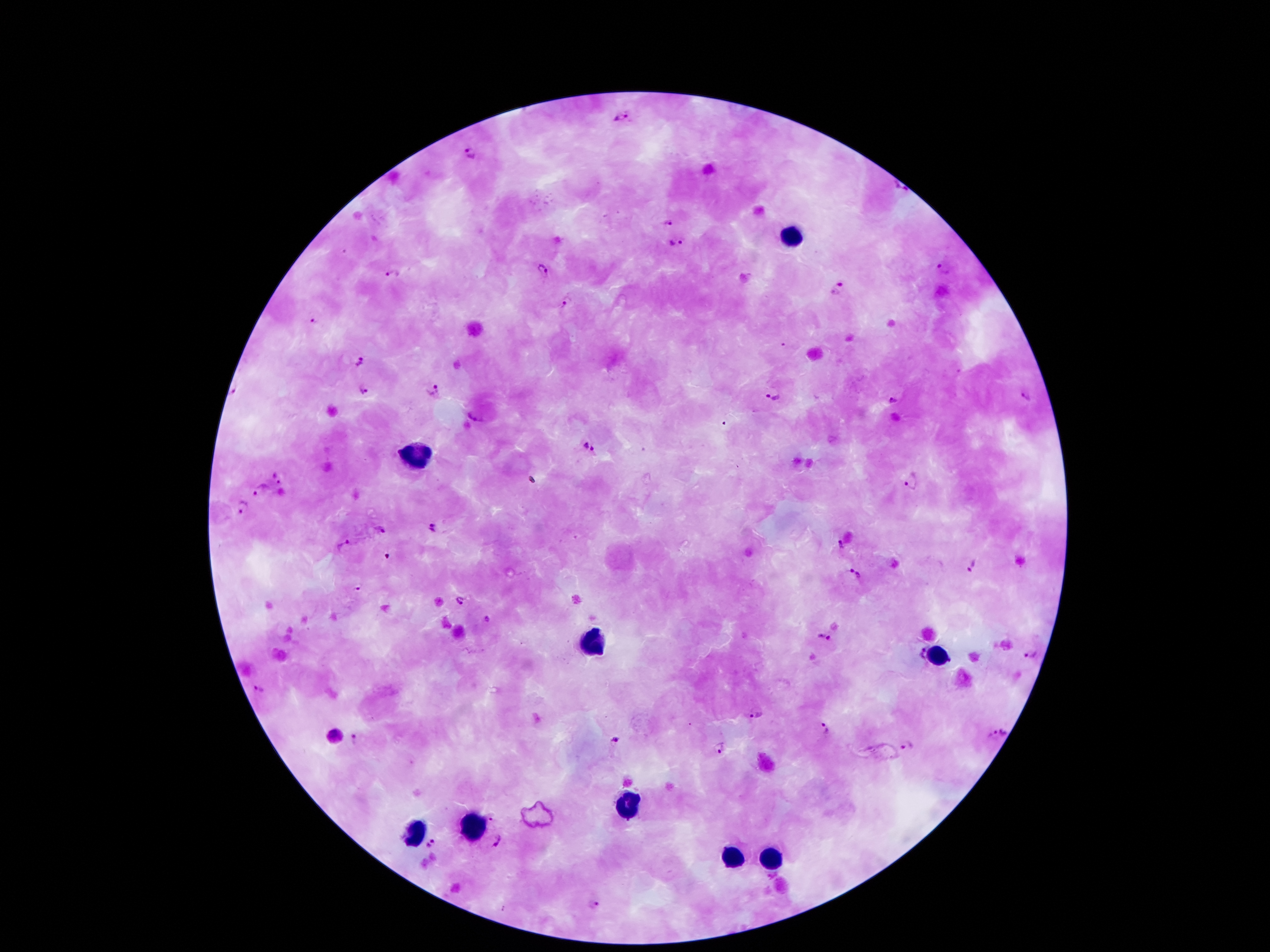

coordinate format = approximate centers as {x, y} in pixels
Plasmodium parasite locations = {621, 118}, {469, 154}, {900, 186}, {666, 223}, {675, 245}, {943, 268}, {541, 269}, {391, 272}, {838, 290}, {567, 301}, {313, 321}, {357, 362}, {364, 390}, {433, 390}, {232, 391}, {1026, 398}, {774, 399}, {892, 402}, {475, 417}, {591, 448}, {279, 477}, {910, 482}, {262, 490}, {241, 507}, {434, 527}, {382, 530}, {343, 546}, {838, 546}, {975, 567}, {854, 575}, {359, 587}, {459, 600}, {487, 622}, {823, 638}, {1030, 656}, {257, 690}, {753, 716}, {824, 728}, {1003, 728}, {613, 738}, {354, 740}, {720, 748}, {493, 817}, {431, 842}, {498, 842}, {594, 904}
leukocyte locations = {791, 235}, {418, 454}, {596, 641}, {934, 651}, {628, 804}, {476, 823}, {411, 832}, {730, 855}, {772, 861}
preparation = thick blood film
image size = 1270×952 pixels
capture = smartphone through the microscope eyepiece
magnification = 100x
patient malaria status = infected with Plasmodium falciparum
stain = Giemsa
field of view = single